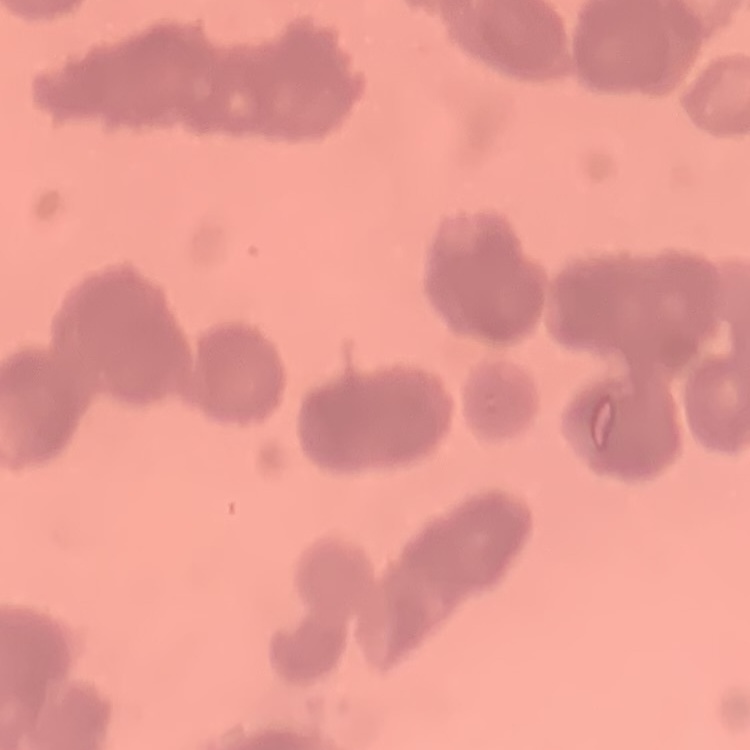
red blood cell morphology = rouleaux formation
image type = square crop of a larger photomicrograph
stain = Field's or Giemsa
preparation = thin blood film